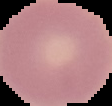

preparation: thin blood smear
image_size: 112×106 pixels
result: no Plasmodium parasites seen
image_type: segmented cell region on a black background